Give the position of every leukocyte visible.
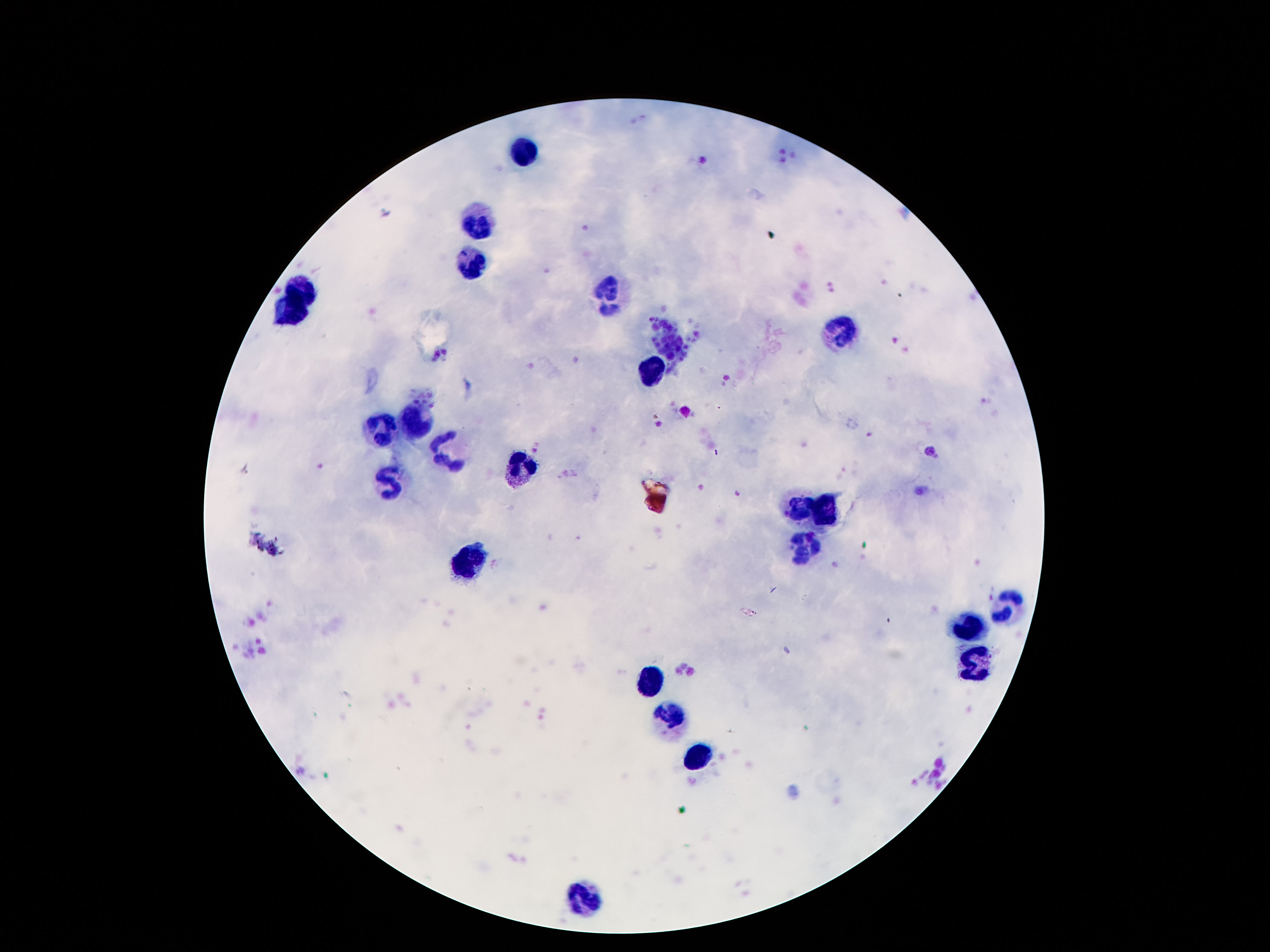

Approximate centers as (x, y) in pixels.
Leukocytes: (525, 155), (478, 223), (470, 263), (301, 289), (609, 292), (287, 316), (841, 329), (650, 373), (416, 418), (386, 432), (448, 450), (518, 469), (389, 485), (798, 506), (827, 512), (802, 547), (477, 559), (1004, 607), (968, 632), (974, 659), (654, 678), (672, 715), (693, 753), (584, 895).

stain = Giemsa
capture = smartphone camera through the microscope eyepiece
preparation = thick peripheral-blood smear
field of view = one from this slide
magnification = 100x
patient malaria status = negative
image size = 1270×952 pixels